Classify this cell by malaria status.
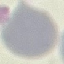

It is uninfected.

Summary:
  - Image type: automatically extracted cell patch, resized to 64 × 64 pixels
  - Capture: smartphone camera at the microscope eyepiece
  - Preparation: thin blood smear
  - Stain: Giemsa